Report the malaria status of this cell.
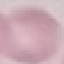

It is uninfected.

image type = cell patch, automatically extracted from a larger field of view and resized to 64 × 64 pixels
preparation = thin blood smear
capture = smartphone through the microscope eyepiece
stain = Giemsa